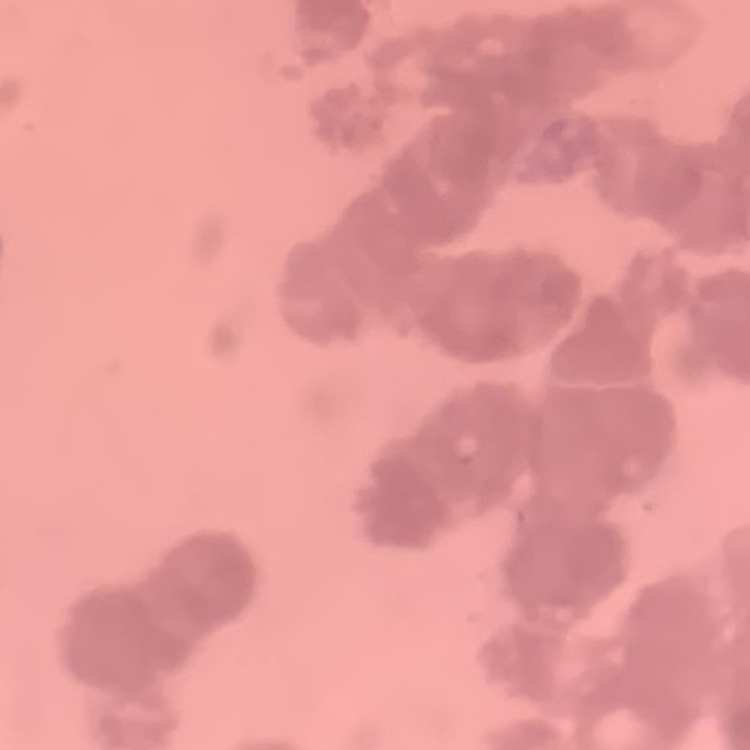

The erythrocytes show rouleaux formation. Square crop of a larger photomicrograph. Stained with either Field's or Giemsa. Thin peripheral smear.